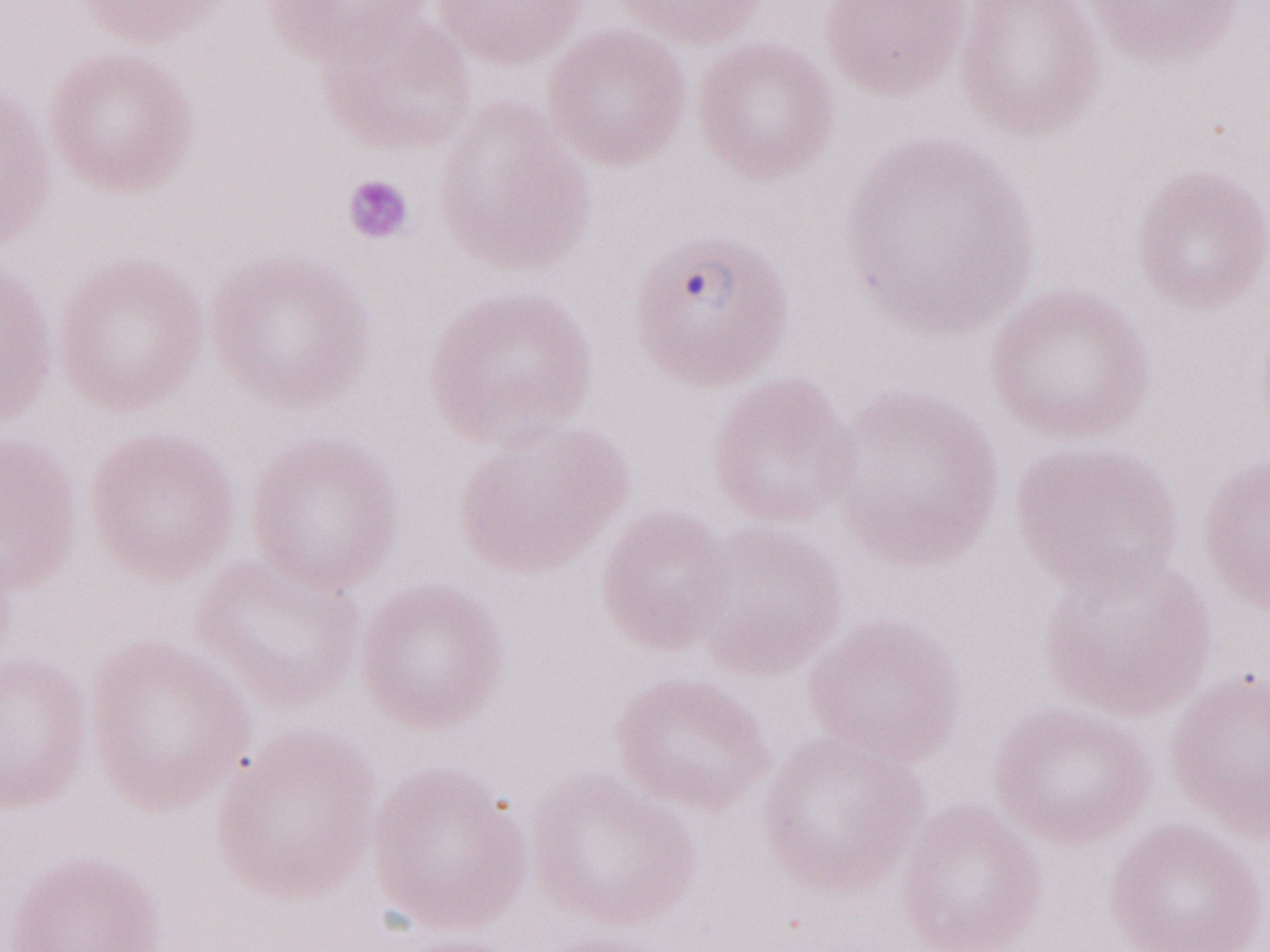

Olympus BX43 microscope, Olympus DP73 camera. One field of this slide. Image is 1270×952 pixels. Patient-level malaria diagnosis: positive. Thin peripheral-blood smear. May-Grünwald-Giemsa-stained preparation. 1,000x magnification.